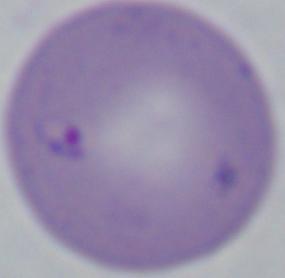
identification = Babesia
modality = photomicrograph
magnification = 1000x